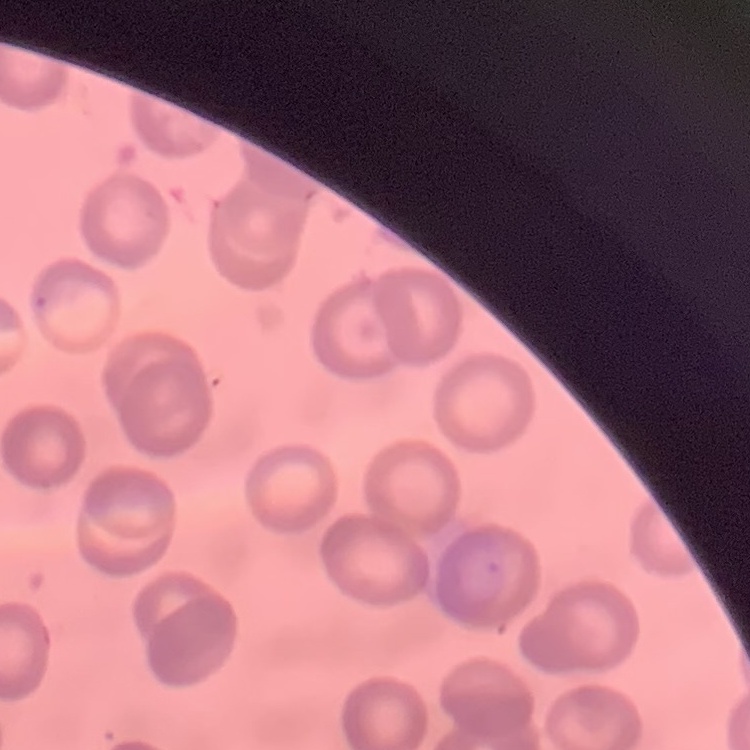

red blood cell morphology = no rouleaux formation
preparation = thin blood smear
image type = square crop of a larger photomicrograph
stain = Field's or Giemsa